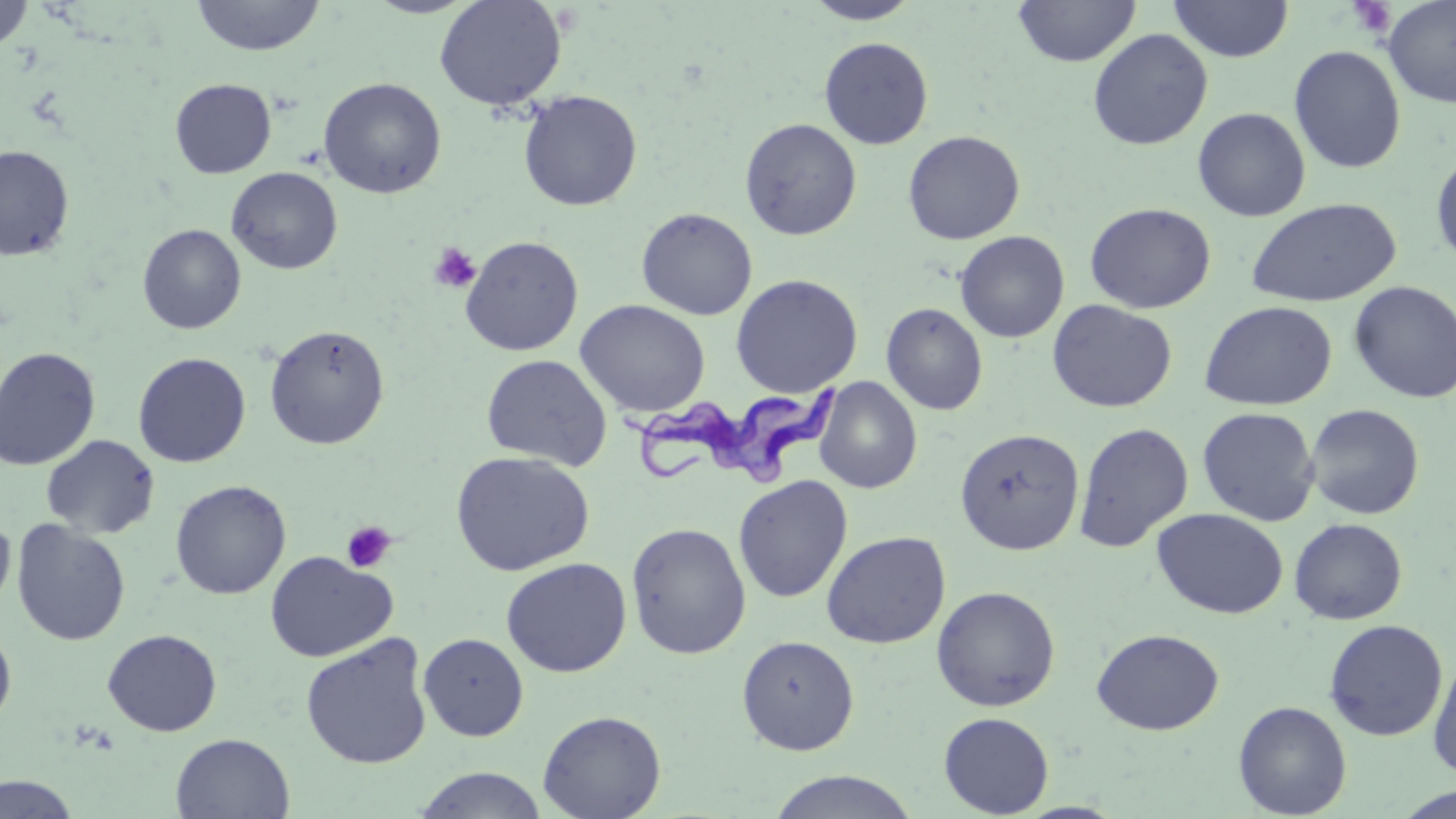
slide-level diagnosis = Trypanosoma brucei
preparation = thin blood smear
modality = light microscopy
platelet locations = approximate bounding boxes as named x1/y1/x2/y2 corners in pixels: (x1=1345, y1=0, x2=1397, y2=38), (x1=428, y1=242, x2=481, y2=293), (x1=341, y1=520, x2=397, y2=574)
stain = May-Grünwald-Giemsa
magnification = 1000x
uninfected red blood cell locations = approximate bounding boxes as named x1/y1/x2/y2 corners in pixels: (x1=191, y1=0, x2=326, y2=57), (x1=434, y1=0, x2=567, y2=111), (x1=1013, y1=0, x2=1141, y2=68), (x1=1167, y1=0, x2=1294, y2=61), (x1=1381, y1=0, x2=1456, y2=109), (x1=1, y1=1, x2=35, y2=53), (x1=803, y1=1, x2=921, y2=24), (x1=1087, y1=28, x2=1213, y2=150), (x1=819, y1=36, x2=934, y2=149), (x1=1288, y1=45, x2=1407, y2=173), (x1=318, y1=77, x2=447, y2=199), (x1=169, y1=78, x2=276, y2=178), (x1=518, y1=90, x2=642, y2=211), (x1=1192, y1=106, x2=1311, y2=221), (x1=739, y1=118, x2=862, y2=240), (x1=902, y1=130, x2=1025, y2=245), (x1=0, y1=145, x2=74, y2=261), (x1=1430, y1=149, x2=1456, y2=270), (x1=226, y1=166, x2=343, y2=274), (x1=1246, y1=197, x2=1402, y2=307), (x1=1084, y1=202, x2=1216, y2=314), (x1=636, y1=207, x2=757, y2=320), (x1=137, y1=224, x2=246, y2=334), (x1=955, y1=231, x2=1069, y2=343), (x1=460, y1=235, x2=583, y2=356), (x1=730, y1=273, x2=863, y2=398), (x1=1348, y1=280, x2=1456, y2=404), (x1=1047, y1=299, x2=1177, y2=413), (x1=575, y1=300, x2=711, y2=417), (x1=1199, y1=300, x2=1338, y2=411), (x1=881, y1=302, x2=988, y2=415), (x1=264, y1=325, x2=390, y2=450), (x1=0, y1=346, x2=100, y2=470), (x1=133, y1=352, x2=251, y2=468), (x1=481, y1=353, x2=613, y2=470), (x1=813, y1=377, x2=922, y2=494), (x1=1304, y1=403, x2=1425, y2=519), (x1=1197, y1=407, x2=1320, y2=527), (x1=1073, y1=422, x2=1194, y2=552), (x1=955, y1=428, x2=1085, y2=555), (x1=41, y1=434, x2=160, y2=539), (x1=451, y1=451, x2=595, y2=576), (x1=733, y1=474, x2=853, y2=603), (x1=170, y1=480, x2=291, y2=600), (x1=1151, y1=507, x2=1289, y2=619), (x1=0, y1=514, x2=15, y2=612), (x1=1289, y1=517, x2=1408, y2=624), (x1=11, y1=519, x2=131, y2=646), (x1=625, y1=521, x2=751, y2=659), (x1=821, y1=530, x2=951, y2=649), (x1=265, y1=550, x2=397, y2=662), (x1=500, y1=557, x2=632, y2=677), (x1=931, y1=586, x2=1061, y2=711), (x1=1323, y1=618, x2=1448, y2=742), (x1=0, y1=624, x2=17, y2=728), (x1=102, y1=628, x2=222, y2=736), (x1=1091, y1=628, x2=1224, y2=734), (x1=418, y1=632, x2=529, y2=741), (x1=300, y1=633, x2=433, y2=769), (x1=737, y1=634, x2=859, y2=755), (x1=1428, y1=651, x2=1456, y2=779), (x1=1233, y1=700, x2=1352, y2=818), (x1=537, y1=709, x2=666, y2=819), (x1=938, y1=712, x2=1055, y2=817), (x1=170, y1=733, x2=295, y2=818), (x1=412, y1=767, x2=549, y2=819), (x1=764, y1=769, x2=923, y2=819), (x1=0, y1=773, x2=83, y2=818), (x1=1395, y1=786, x2=1456, y2=819)
Trypanosoma brucei locations = approximate bounding boxes as named x1/y1/x2/y2 corners in pixels: (x1=615, y1=374, x2=848, y2=488)
field of view = one of a larger specimen
image size = 1456×819 pixels